State the preparation type.
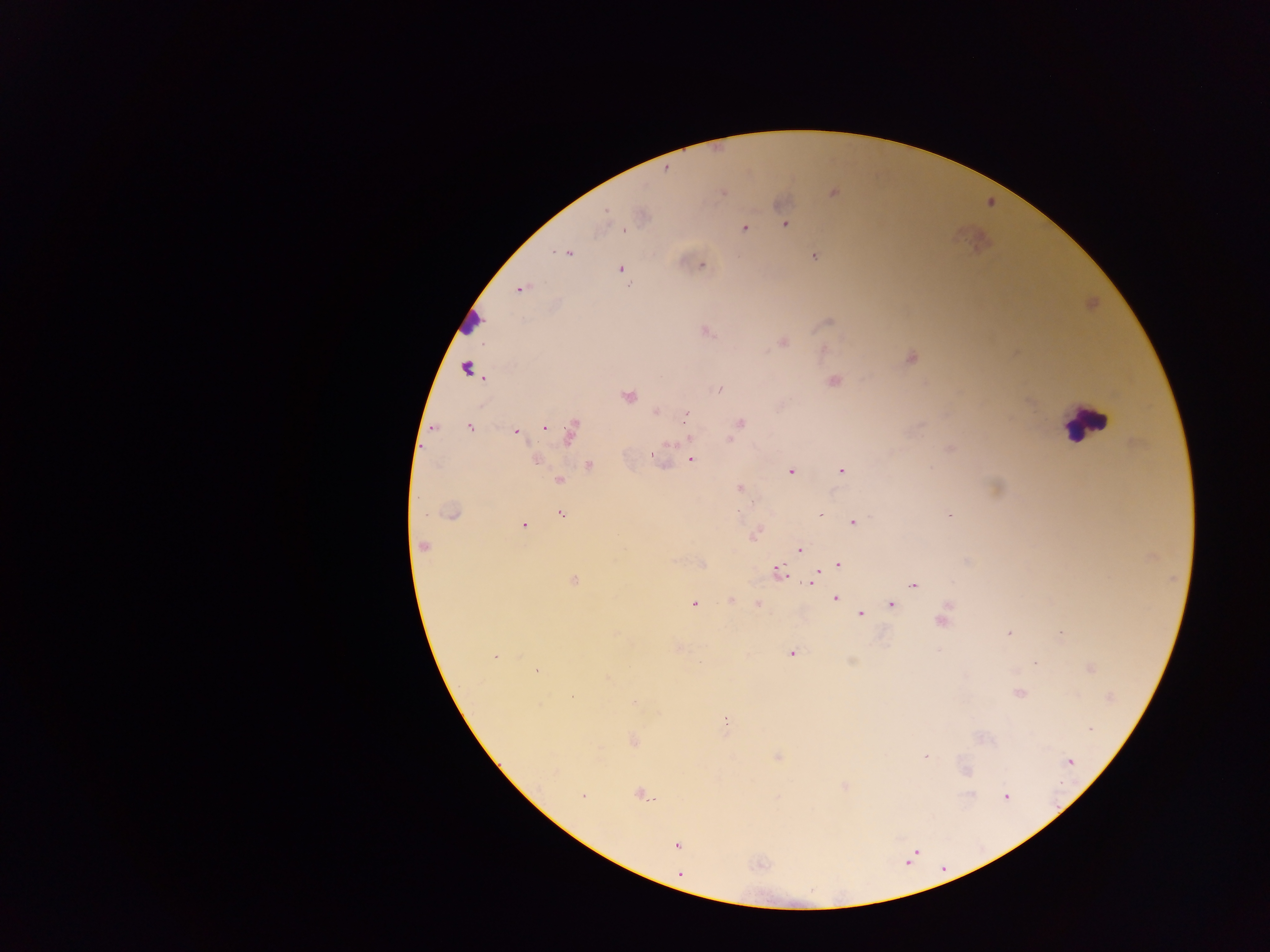

Thick blood smear.

Approximate centers as [x, y] in pixels. Plasmodium parasite locations: [666, 169], [722, 192], [834, 192], [606, 212], [642, 215], [785, 224], [744, 228], [568, 253], [814, 256], [702, 265], [620, 269], [522, 288], [828, 323], [706, 332], [783, 342], [911, 357], [466, 367], [834, 381], [719, 389], [628, 396], [655, 412], [686, 413], [741, 422], [469, 427], [545, 428], [516, 432], [570, 432], [689, 439], [730, 440], [535, 459], [691, 459], [590, 466], [840, 470], [791, 471], [560, 480], [740, 488], [425, 514], [452, 514], [562, 514], [820, 514], [853, 523], [525, 525], [754, 535], [423, 546], [800, 548], [702, 564], [838, 564], [779, 570], [815, 575], [574, 580], [812, 582], [913, 585], [835, 597], [731, 601], [694, 604], [758, 605], [891, 605], [860, 614], [942, 621], [1010, 633], [1061, 634], [792, 654], [494, 657], [1035, 663], [536, 670], [1020, 693], [571, 697], [726, 722], [1089, 729], [633, 740], [926, 757], [1070, 761], [967, 772], [844, 787], [640, 794], [582, 795], [970, 795], [1006, 797], [677, 845], [680, 874]. Leukocyte locations: [1085, 423]. Image is 1270×952 pixels. Single field of view. Sample from Ghana. Photographed through a microscope with a mobile-phone camera.